Identify the blood parasite species.
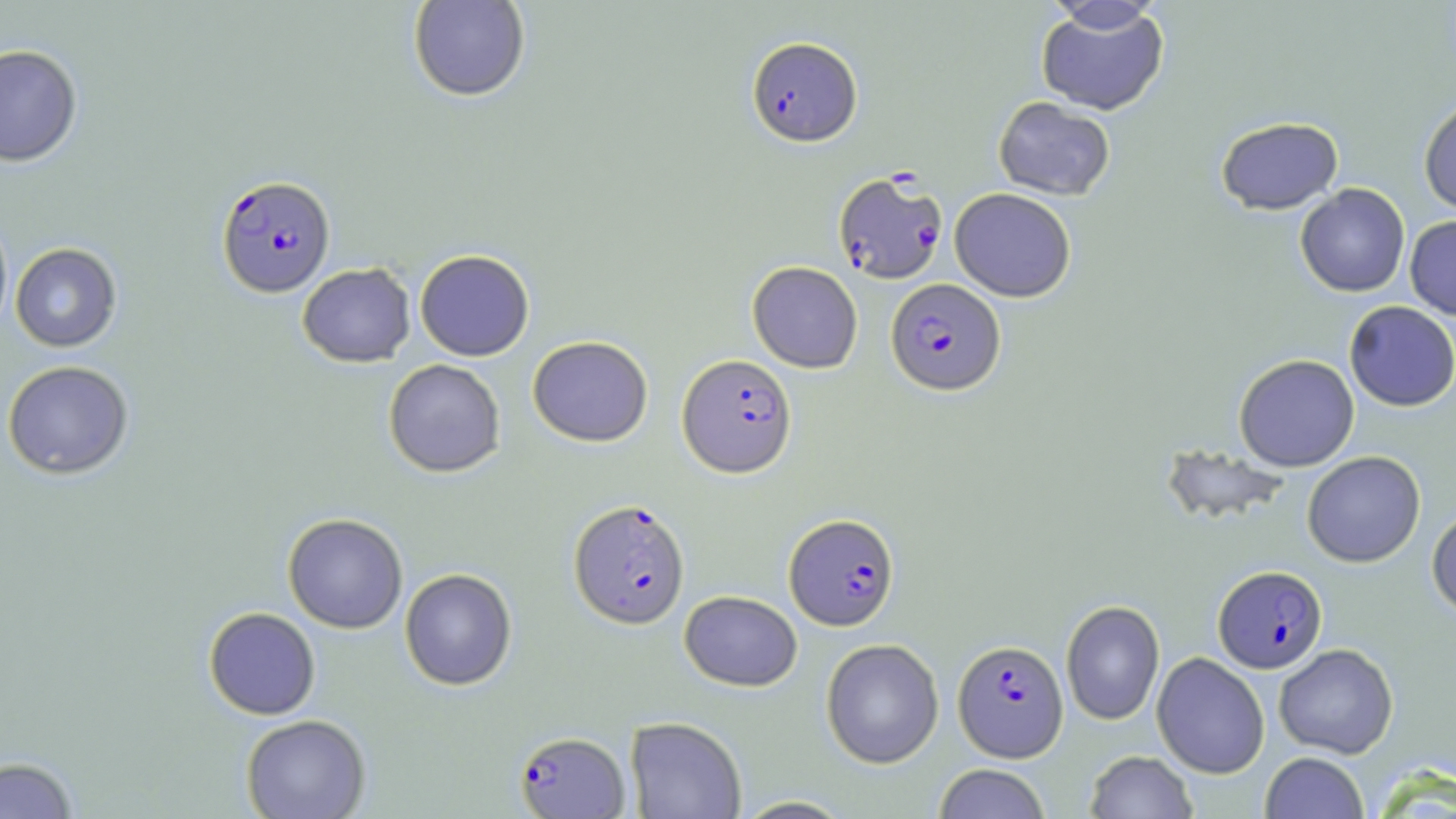

Plasmodium falciparum.

Approximate bounding boxes as named x1/y1/x2/y2 corners in pixels. Uninfected red blood cell locations: (x1=408, y1=0, x2=531, y2=103), (x1=1041, y1=1, x2=1167, y2=35), (x1=1035, y1=3, x2=1169, y2=116), (x1=0, y1=43, x2=83, y2=167), (x1=993, y1=96, x2=1115, y2=200), (x1=1418, y1=98, x2=1456, y2=216), (x1=1215, y1=116, x2=1344, y2=215), (x1=1295, y1=184, x2=1410, y2=297), (x1=950, y1=188, x2=1076, y2=302), (x1=0, y1=207, x2=13, y2=342), (x1=1405, y1=215, x2=1456, y2=320), (x1=10, y1=242, x2=122, y2=352), (x1=415, y1=249, x2=534, y2=361), (x1=747, y1=261, x2=863, y2=373), (x1=297, y1=263, x2=416, y2=367), (x1=1344, y1=301, x2=1456, y2=412), (x1=527, y1=335, x2=653, y2=446), (x1=1234, y1=354, x2=1360, y2=471), (x1=384, y1=358, x2=506, y2=478), (x1=2, y1=360, x2=134, y2=479), (x1=1158, y1=442, x2=1293, y2=528), (x1=1302, y1=451, x2=1426, y2=567), (x1=1427, y1=506, x2=1456, y2=618), (x1=282, y1=513, x2=408, y2=633), (x1=400, y1=568, x2=517, y2=690), (x1=679, y1=590, x2=802, y2=691), (x1=1060, y1=599, x2=1165, y2=726), (x1=203, y1=607, x2=320, y2=719), (x1=821, y1=638, x2=944, y2=768), (x1=1274, y1=643, x2=1398, y2=759), (x1=1151, y1=652, x2=1270, y2=778), (x1=241, y1=714, x2=371, y2=819), (x1=625, y1=716, x2=747, y2=819), (x1=1085, y1=750, x2=1198, y2=819), (x1=1260, y1=752, x2=1369, y2=818), (x1=0, y1=755, x2=79, y2=818), (x1=933, y1=763, x2=1051, y2=819), (x1=729, y1=795, x2=857, y2=818). Plasmodium falciparum-infected red blood cell locations: (x1=746, y1=36, x2=862, y2=147), (x1=833, y1=171, x2=948, y2=285), (x1=216, y1=174, x2=336, y2=297), (x1=885, y1=278, x2=1005, y2=396), (x1=677, y1=354, x2=796, y2=478), (x1=568, y1=498, x2=690, y2=629), (x1=784, y1=512, x2=900, y2=631), (x1=1213, y1=565, x2=1327, y2=673), (x1=953, y1=639, x2=1068, y2=762), (x1=514, y1=730, x2=631, y2=818). May-Grünwald-Giemsa stain. Image is 1456×819 pixels. Light microscopy. Captured at 1000x magnification. Thin blood film. Single field of view.